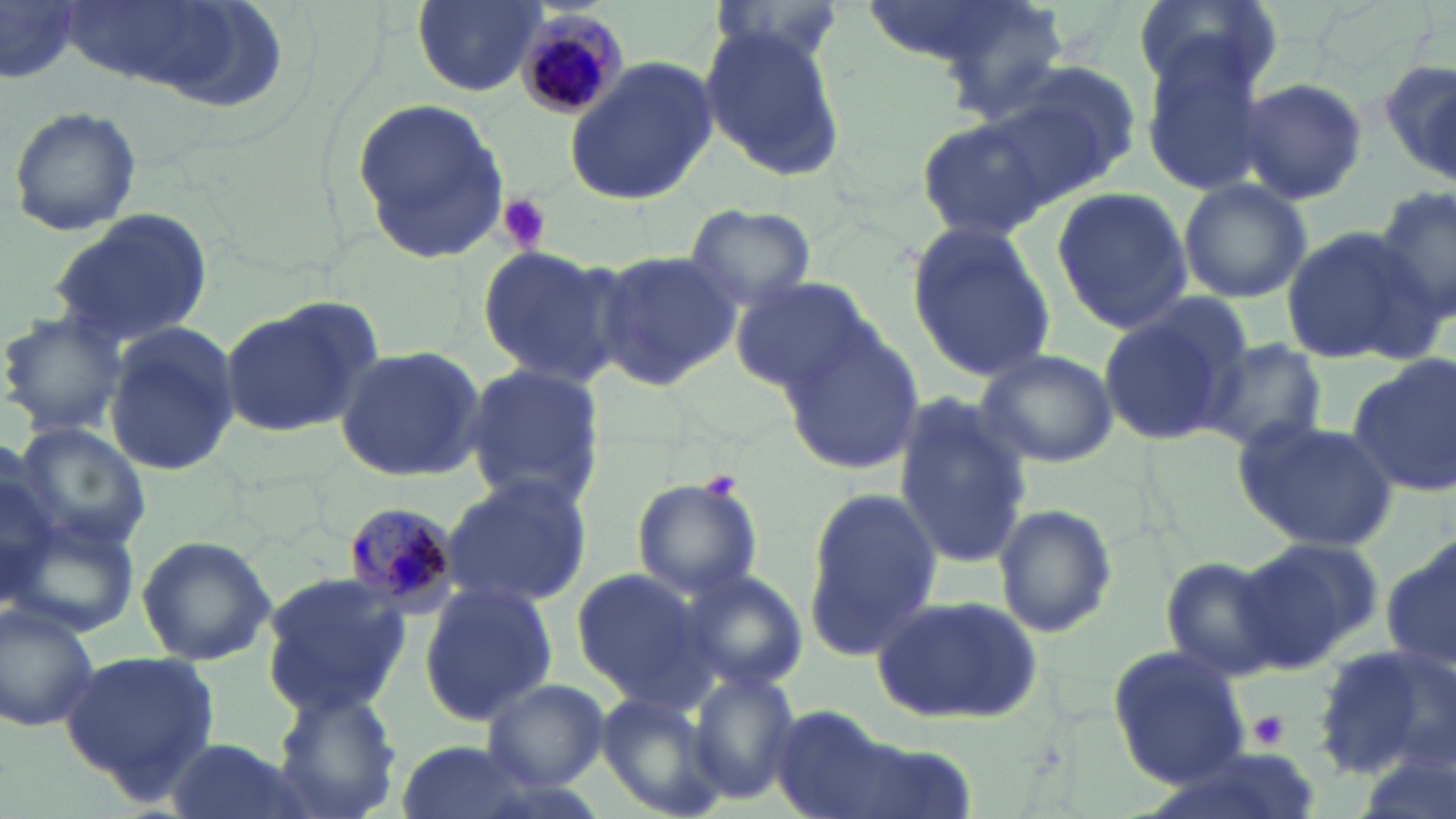
Summary:
  - Coordinate format: approximate bounding boxes as (x1,y1)-(x2,y2) corner pairs in pixels
  - Uninfected red blood cell locations: (410,0)-(544,97), (855,0)-(1057,78), (1134,0)-(1277,97), (1,3)-(86,86), (697,23)-(847,180), (1139,39)-(1272,196), (563,60)-(717,207), (1379,60)-(1456,186), (975,70)-(1134,211), (1236,78)-(1369,208), (352,99)-(514,262), (7,104)-(143,236), (915,114)-(1057,245), (1177,178)-(1312,303), (1374,184)-(1455,332), (1051,186)-(1193,335), (684,203)-(817,312), (45,209)-(215,349), (906,220)-(1058,382), (1280,225)-(1427,364), (474,242)-(625,389), (593,248)-(742,394), (731,275)-(879,395), (1095,298)-(1247,446), (220,300)-(380,437), (0,312)-(128,437), (105,321)-(242,478), (783,323)-(923,475), (1200,336)-(1327,455), (333,344)-(487,480), (975,349)-(1118,467), (1348,357)-(1456,498), (462,363)-(606,512), (894,394)-(1036,565), (1236,416)-(1401,551), (13,422)-(155,553), (0,448)-(60,611), (439,474)-(594,610), (631,475)-(763,600), (802,485)-(943,659), (994,502)-(1118,640), (10,505)-(143,641), (135,534)-(277,667), (1383,536)-(1456,679), (1243,537)-(1384,666), (1158,555)-(1291,680), (569,569)-(714,706), (676,569)-(808,694), (258,571)-(411,717), (418,582)-(555,726), (872,592)-(1042,723), (1,602)-(101,733), (1311,641)-(1454,778), (1106,645)-(1250,790), (60,649)-(223,801), (689,668)-(800,805), (480,677)-(610,788), (270,686)-(403,819), (596,688)-(727,819), (765,703)-(893,819), (163,736)-(311,819), (388,739)-(547,819)
  - Plasmodium malariae-infected red blood cell locations: (515,12)-(625,122), (338,501)-(461,618)
  - Platelet locations: (495,193)-(551,255), (702,469)-(743,502), (1250,711)-(1287,749)
  - Slide-level diagnosis: Plasmodium malariae
  - Stain: May-Grünwald-Giemsa
  - Field of view: single
  - Image size: 1456×819 pixels
  - Modality: light microscopy
  - Preparation: thin blood smear
  - Magnification: 1000x